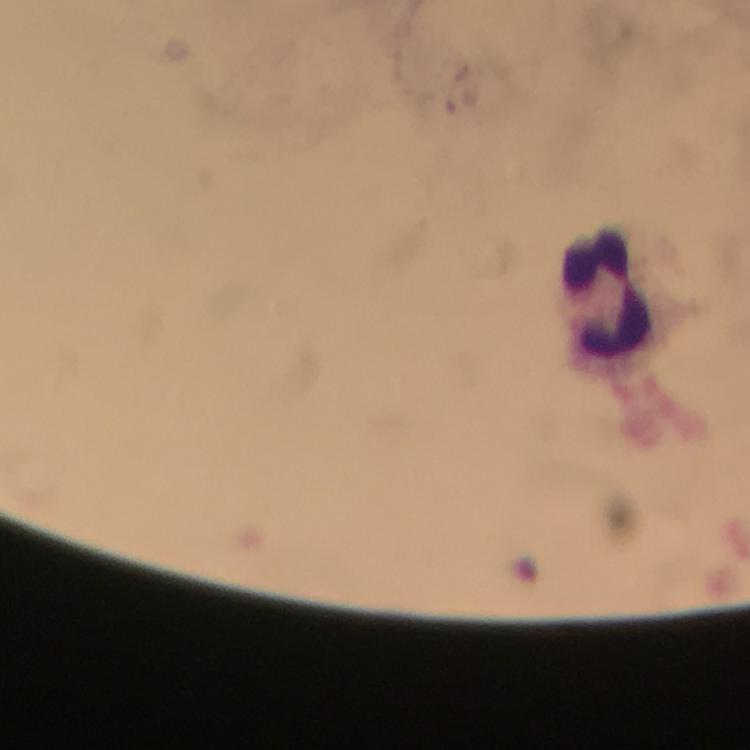
Approximate centers as (x, y) in pixels. Leukocyte locations: (608, 292). Thick blood smear. Plasmodium parasites: none detected. Image is 750×750 pixels. Cropped region of a single field of view. At 100x magnification. Immersion oil was used. Giemsa-stained preparation. Photographed with a smartphone mounted on the microscope. From a diagnostic examination for malaria.